Name the blood parasite species.
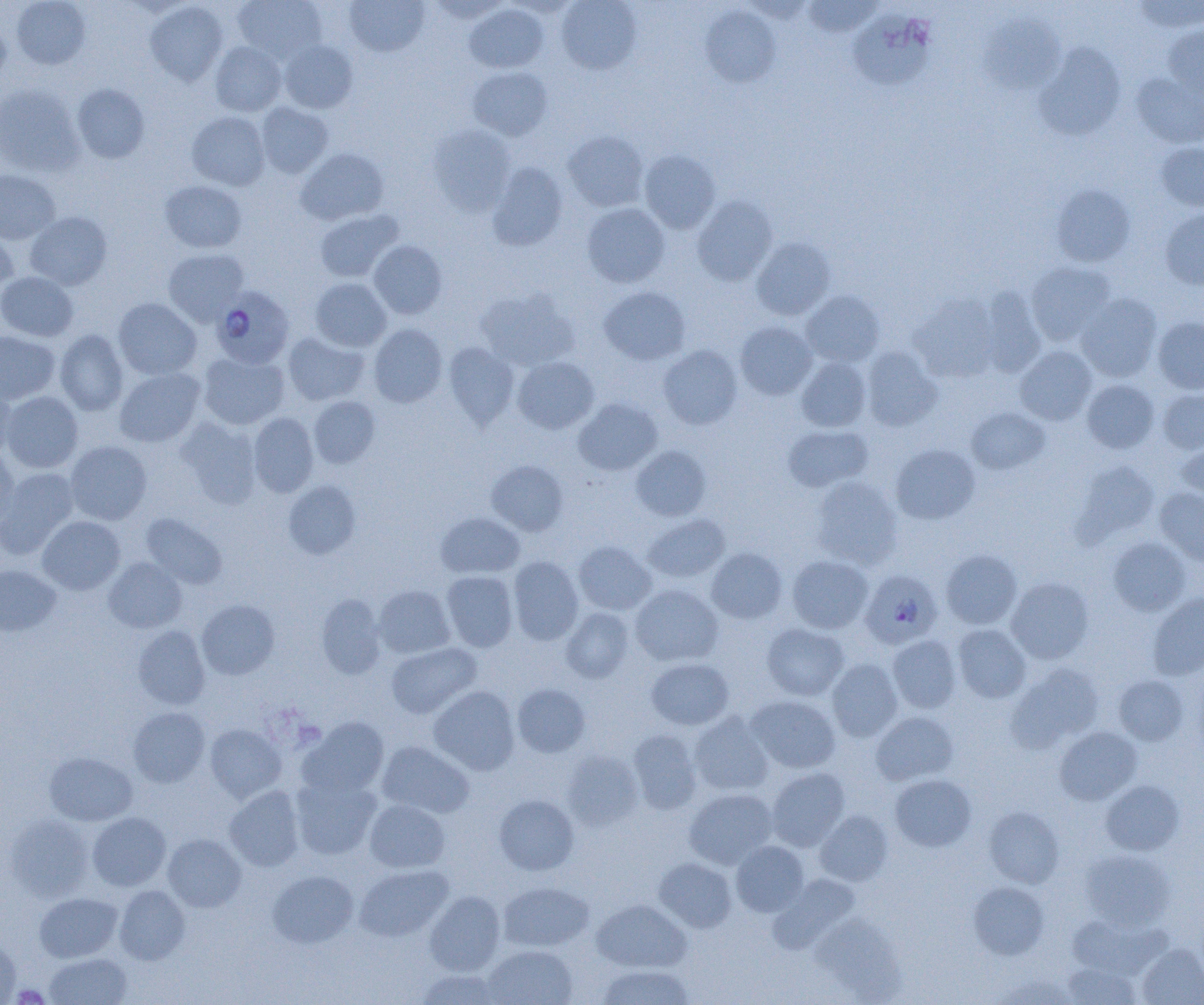
Plasmodium falciparum.

Summary:
  - Coordinate format: approximate bounding boxes as (x1, y1, x2, y2) in pixels
  - Platelet locations: (12, 984, 49, 1004)
  - Uninfected red blood cell locations: (11, 0, 91, 69), (233, 0, 326, 62), (344, 0, 428, 56), (427, 0, 511, 22), (557, 0, 641, 74), (803, 0, 882, 38), (1134, 0, 1204, 33), (145, 2, 228, 85), (464, 4, 548, 74), (701, 5, 780, 88), (848, 9, 936, 91), (981, 15, 1064, 94), (0, 20, 11, 89), (1163, 24, 1204, 100), (278, 39, 358, 114), (210, 42, 287, 116), (1035, 43, 1126, 141), (468, 66, 553, 141), (1132, 73, 1204, 148), (0, 84, 83, 176), (72, 84, 150, 163), (255, 103, 333, 178), (187, 111, 270, 190), (428, 124, 516, 215), (563, 131, 648, 212), (1155, 142, 1204, 211), (295, 148, 389, 225), (639, 150, 720, 234), (487, 162, 568, 250), (0, 169, 60, 244), (160, 180, 246, 252), (1051, 184, 1135, 267), (692, 195, 778, 286), (582, 203, 670, 288), (314, 209, 402, 282), (1160, 209, 1204, 290), (25, 212, 112, 290), (0, 230, 18, 298), (751, 237, 836, 321), (368, 240, 447, 319), (163, 248, 248, 325), (1026, 261, 1116, 346), (0, 271, 79, 341), (309, 278, 391, 352), (599, 286, 691, 365), (979, 287, 1046, 377), (475, 288, 578, 370), (802, 291, 885, 366), (1076, 293, 1162, 382), (909, 294, 1001, 382), (114, 298, 201, 379), (1153, 317, 1204, 394), (735, 321, 817, 400), (369, 324, 448, 407), (55, 329, 128, 416), (0, 331, 60, 404), (283, 332, 369, 405), (443, 343, 520, 428), (659, 345, 742, 429), (1015, 346, 1097, 425), (861, 347, 942, 431), (198, 351, 289, 430), (512, 356, 599, 434), (796, 356, 872, 432), (114, 368, 205, 447), (1082, 379, 1159, 454), (0, 382, 17, 458), (1157, 387, 1204, 454), (1, 391, 83, 473), (308, 396, 380, 469), (574, 398, 662, 475), (967, 407, 1051, 475), (248, 412, 319, 497), (176, 418, 261, 508), (782, 425, 873, 492), (65, 441, 152, 525), (1176, 443, 1204, 510), (891, 444, 980, 524), (631, 445, 711, 521), (0, 448, 20, 532), (486, 459, 569, 536), (1075, 461, 1160, 543), (0, 467, 78, 556), (810, 476, 902, 569), (282, 480, 361, 559), (1155, 487, 1204, 567), (435, 512, 525, 578), (141, 513, 227, 589), (643, 514, 730, 583), (37, 516, 125, 595), (1108, 537, 1191, 616), (574, 541, 656, 615), (706, 548, 787, 624), (941, 549, 1022, 629), (787, 555, 873, 633), (508, 556, 583, 645), (103, 557, 187, 633), (0, 565, 61, 636), (441, 571, 517, 652), (1006, 577, 1094, 664), (630, 584, 723, 666), (374, 585, 455, 658), (1147, 593, 1204, 679), (315, 595, 386, 679), (197, 599, 279, 680), (561, 606, 635, 683), (761, 624, 849, 700), (952, 624, 1031, 703), (133, 625, 210, 710), (887, 634, 962, 713), (386, 642, 482, 718), (646, 658, 734, 729), (827, 658, 903, 742), (1008, 662, 1104, 751), (1113, 674, 1188, 745), (512, 683, 591, 758), (428, 686, 520, 775), (746, 695, 840, 773), (128, 707, 210, 786), (871, 711, 959, 785), (688, 712, 774, 796), (299, 716, 389, 797), (205, 724, 286, 803), (1054, 726, 1142, 804), (628, 729, 703, 814), (377, 741, 474, 818), (561, 750, 644, 831), (44, 751, 138, 825), (766, 768, 849, 850), (290, 774, 381, 860), (889, 774, 976, 852), (1100, 779, 1184, 855), (224, 786, 305, 871), (684, 788, 777, 869), (494, 794, 579, 875), (364, 799, 450, 873), (984, 806, 1064, 888), (815, 810, 893, 886), (87, 812, 170, 891), (4, 813, 94, 900), (163, 833, 246, 912), (731, 841, 809, 916), (1080, 849, 1175, 930), (654, 857, 736, 932), (354, 864, 453, 941), (267, 869, 358, 949), (768, 874, 860, 953), (498, 881, 594, 952), (968, 881, 1049, 959), (114, 885, 190, 965), (425, 890, 505, 974), (35, 892, 122, 962), (592, 899, 691, 972), (812, 916, 902, 997), (0, 937, 20, 1004), (1136, 943, 1204, 1005), (482, 944, 577, 1005), (45, 953, 132, 1004), (1063, 962, 1140, 1004), (595, 964, 695, 1005), (415, 969, 504, 1005), (992, 973, 1078, 1004)
  - Plasmodium falciparum-infected red blood cell locations: (211, 286, 295, 368), (860, 570, 942, 649)
  - Field of view: one of a larger specimen
  - Image size: 1204×1005 pixels
  - Magnification: 1000x
  - Modality: optical microscopy
  - Preparation: thin blood film